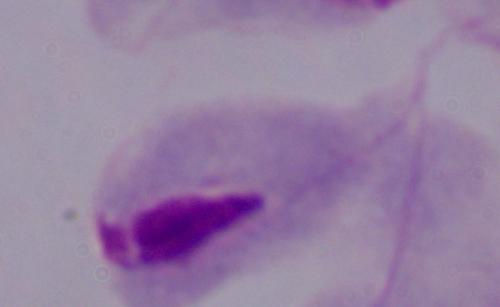

Summary:
  - Magnification: 1000x
  - Identification: trichomonad
  - Modality: micrograph